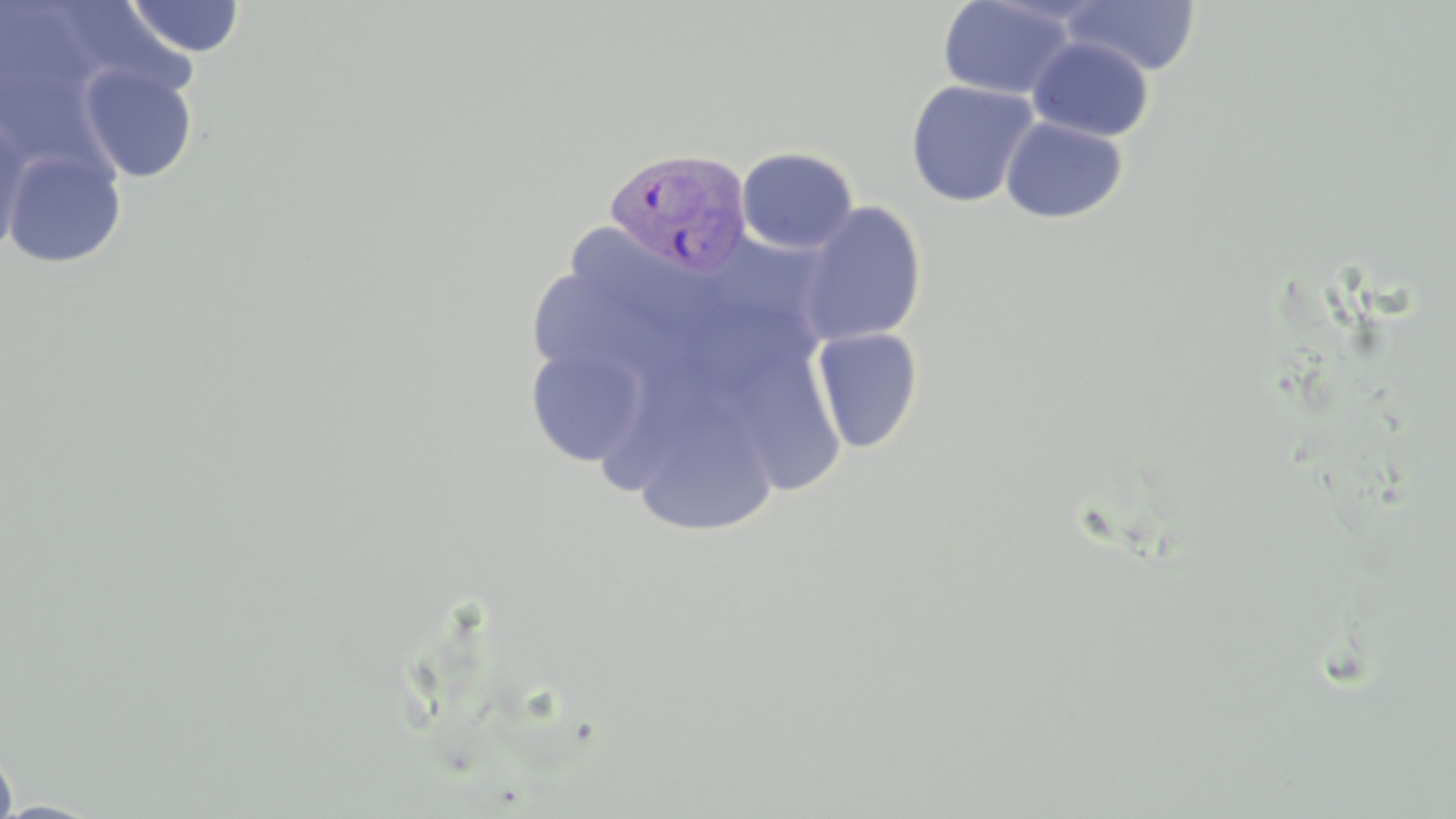

slide_level_diagnosis: Plasmodium vivax
image_size: 1456×819 pixels
stain: May-Grünwald-Giemsa
magnification: 1000x
field_of_view: one of a larger specimen
uninfected_red_blood_cell_locations: 'approximate bounding boxes as (x1, y1, x2, y2) in pixels: (124, 0, 246, 58), (938, 0, 1079, 99), (1062, 0, 1201, 75), (1026, 35, 1154, 141), (78, 63, 199, 183), (905, 79, 1040, 208), (0, 114, 31, 254), (1000, 116, 1128, 224), (736, 147, 859, 255), (3, 148, 127, 268), (795, 201, 928, 347), (567, 223, 727, 342), (531, 273, 694, 375), (810, 327, 924, 453), (524, 342, 649, 468), (736, 344, 854, 505), (650, 383, 776, 541), (0, 735, 19, 819)'
modality: light microscopy
preparation: thin blood film
plasmodium_vivax_infected_red_blood_cell_locations: 'approximate bounding boxes as (x1, y1, x2, y2) in pixels: (604, 146, 753, 277)'